Classify this cell by malaria status.
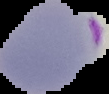

It is parasitized.

preparation = thin blood smear
image size = 109×94 pixels
image type = segmented cell region with the area outside set to black